Name the parasite shown.
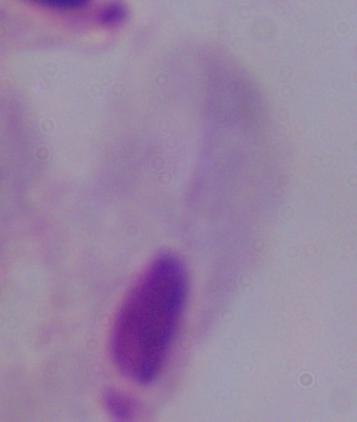
This is a trichomonad.

Photomicrograph. 1000x magnification.